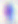

Summary:
  - Modality: micrograph
  - Identification: Toxoplasma gondii
  - Magnification: 400x